Outline each blood parasite and name the species.
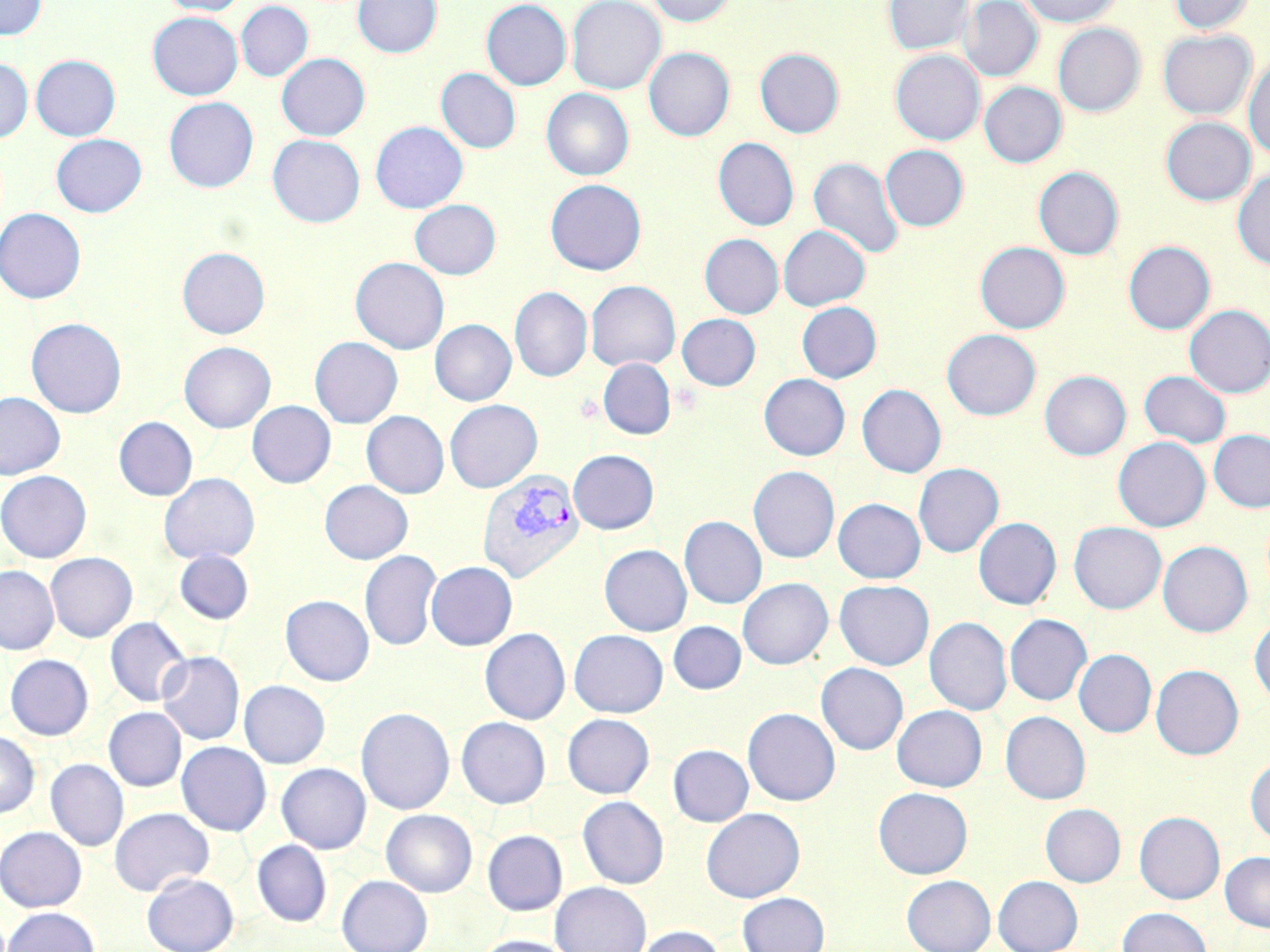

Approximate bounding boxes as (x1, y1, x2, y2) in pixels.
Plasmodium vivax-infected red blood cells: (477, 468, 585, 584).
No Plasmodium falciparum, Plasmodium ovale, Plasmodium malariae, Babesia divergens, or Trypanosoma brucei observed.

Summary:
  - Uninfected red blood cell locations: (0, 0, 47, 39), (159, 0, 248, 16), (353, 0, 441, 58), (481, 0, 572, 90), (566, 0, 665, 94), (647, 0, 737, 26), (883, 0, 974, 55), (959, 0, 1042, 81), (1021, 0, 1122, 27), (1169, 0, 1255, 34), (236, 1, 313, 81), (147, 12, 243, 100), (1052, 24, 1145, 116), (1158, 30, 1256, 119), (644, 47, 734, 141), (754, 48, 844, 138), (890, 50, 984, 145), (276, 53, 370, 140), (31, 55, 120, 141), (1244, 55, 1270, 161), (0, 58, 33, 142), (436, 68, 521, 153), (979, 82, 1066, 167), (541, 88, 634, 180), (164, 96, 258, 193), (1160, 117, 1256, 205), (370, 121, 468, 213), (51, 133, 146, 217), (268, 134, 365, 227), (713, 137, 798, 231), (880, 145, 968, 231), (808, 156, 904, 259), (1033, 166, 1124, 260), (1232, 169, 1270, 270), (545, 179, 646, 275), (410, 199, 501, 279), (0, 208, 86, 304), (778, 225, 870, 310), (700, 234, 783, 318), (975, 241, 1070, 334), (1123, 241, 1215, 334), (177, 247, 270, 338), (350, 257, 449, 354), (585, 280, 680, 372), (510, 286, 592, 381), (797, 301, 881, 383), (1184, 305, 1270, 398), (677, 314, 761, 390), (26, 317, 126, 418), (430, 319, 516, 405), (942, 329, 1040, 420), (309, 336, 403, 428), (179, 341, 275, 433), (598, 358, 676, 440), (1040, 370, 1130, 460), (1139, 370, 1231, 448), (758, 373, 850, 460), (857, 384, 946, 478), (0, 391, 65, 480), (444, 399, 543, 493), (247, 401, 336, 487), (361, 411, 448, 498), (113, 417, 198, 500), (1209, 430, 1270, 511), (1113, 437, 1210, 531), (568, 449, 659, 534), (913, 463, 1003, 558), (748, 466, 839, 563), (0, 471, 91, 563), (159, 472, 260, 564), (319, 480, 413, 564), (833, 498, 925, 583), (679, 516, 766, 608), (973, 517, 1061, 609), (1069, 521, 1166, 613), (1157, 541, 1252, 637), (599, 544, 692, 636), (174, 550, 254, 624), (360, 550, 442, 651), (45, 552, 137, 642), (426, 561, 517, 651), (0, 565, 59, 655), (738, 578, 832, 669), (826, 579, 917, 753), (834, 580, 934, 670), (280, 594, 374, 686), (1005, 614, 1092, 705), (106, 616, 191, 707), (925, 617, 1011, 715), (1249, 620, 1270, 706), (668, 621, 746, 694), (480, 628, 570, 724), (568, 629, 668, 717), (1074, 649, 1156, 737), (157, 651, 244, 745), (5, 654, 93, 739), (816, 662, 908, 754), (1151, 665, 1244, 759), (239, 680, 330, 768), (892, 705, 987, 792), (104, 707, 187, 791), (356, 707, 455, 815), (742, 707, 840, 805), (1000, 711, 1090, 804), (562, 713, 655, 798), (456, 717, 551, 808), (0, 731, 40, 818), (176, 741, 272, 835), (668, 744, 753, 826), (1245, 756, 1270, 844), (46, 759, 129, 850), (276, 763, 371, 853), (873, 787, 973, 878), (577, 796, 669, 889), (1040, 804, 1126, 887), (109, 807, 214, 896), (701, 807, 804, 902), (381, 809, 477, 897), (1134, 811, 1224, 904), (0, 827, 87, 912), (482, 830, 567, 915), (252, 840, 331, 927), (1220, 851, 1270, 932), (141, 873, 239, 952), (336, 875, 433, 952), (901, 875, 995, 952), (993, 875, 1082, 952), (549, 882, 651, 952), (737, 892, 830, 952), (2, 906, 100, 952), (1117, 907, 1212, 952), (635, 925, 727, 952), (472, 935, 578, 952)
  - Slide-level diagnosis: Plasmodium vivax
  - Image size: 1270×952 pixels
  - Preparation: thin blood film
  - Stain: May-Grünwald-Giemsa
  - Magnification: 1000x
  - Modality: optical microscopy
  - Field of view: single